Classify this cell by malaria status.
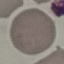

Uninfected.

image type = automatically extracted cell patch, resized to 64 × 64 pixels
preparation = thin blood smear
stain = Giemsa
capture = smartphone through the microscope eyepiece